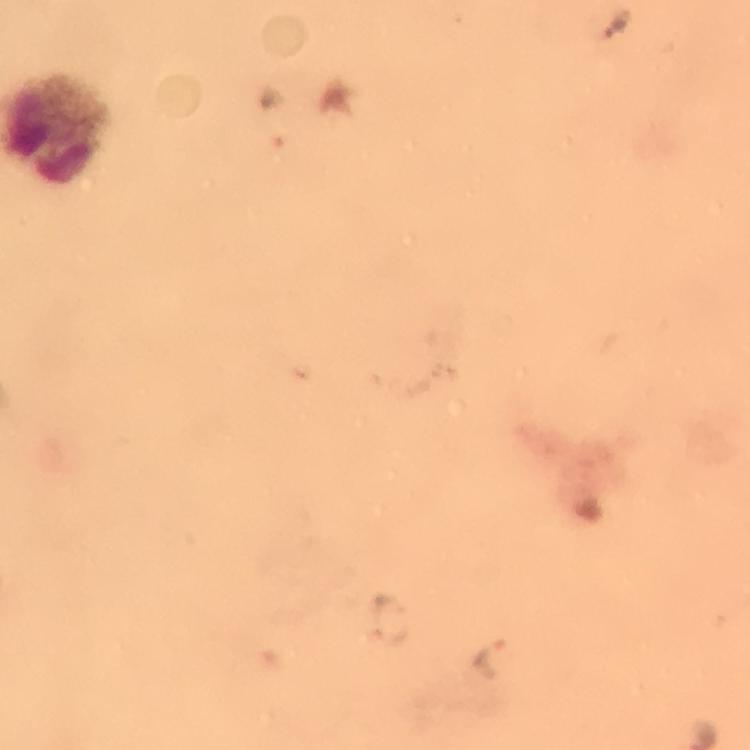

Approximate centers as [x, y] in pixels.
Summary:
  - Plasmodium parasite locations: [617, 23], [489, 658]
  - Leukocyte locations: [55, 127]
  - Immersion oil: used
  - Cropped from: one field of view
  - Context: from a malaria diagnostic workup
  - Image size: 750×750 pixels
  - Capture: smartphone photograph through a microscope
  - Magnification: 100x
  - Stain: Giemsa
  - Preparation: thick blood film